Report the malaria status of this cell.
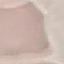
Uninfected.

Summary:
  - Capture: smartphone through the microscope eyepiece
  - Image type: cell patch, automatically extracted from a larger field of view and resized to 64 × 64 pixels
  - Stain: Giemsa
  - Preparation: thin blood smear